Identify the parasite.
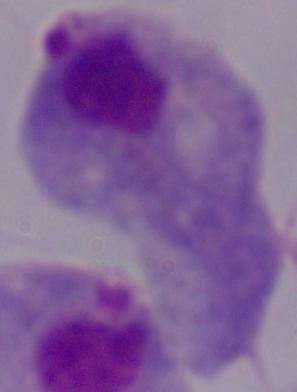

This is a trichomonad.

magnification = 1000x
modality = micrograph